Name the parasite shown.
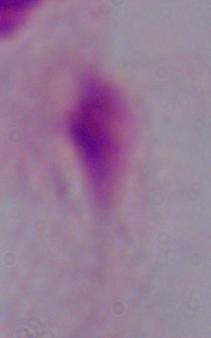

A trichomonad.

Summary:
  - Modality: micrograph
  - Magnification: 1000x